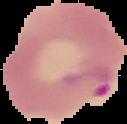
{
  "preparation": "thin blood film",
  "image_type": "segmented cell region on a black background",
  "image_size": "127×124 pixels",
  "malaria_status": "parasitized"
}